Assess this cell for malaria.
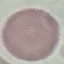

It is uninfected.

preparation = thin blood smear
stain = Giemsa
capture = smartphone through the microscope eyepiece
image type = cell patch, automatically extracted from a larger field of view and resized to 64 × 64 pixels